Classify this cell by malaria status.
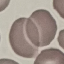

It is uninfected.

image_type: cell patch, automatically extracted from a larger field of view and resized to 64 × 64 pixels
capture: smartphone camera at the microscope eyepiece
stain: Giemsa
preparation: thin blood smear